Mark where platelets are.
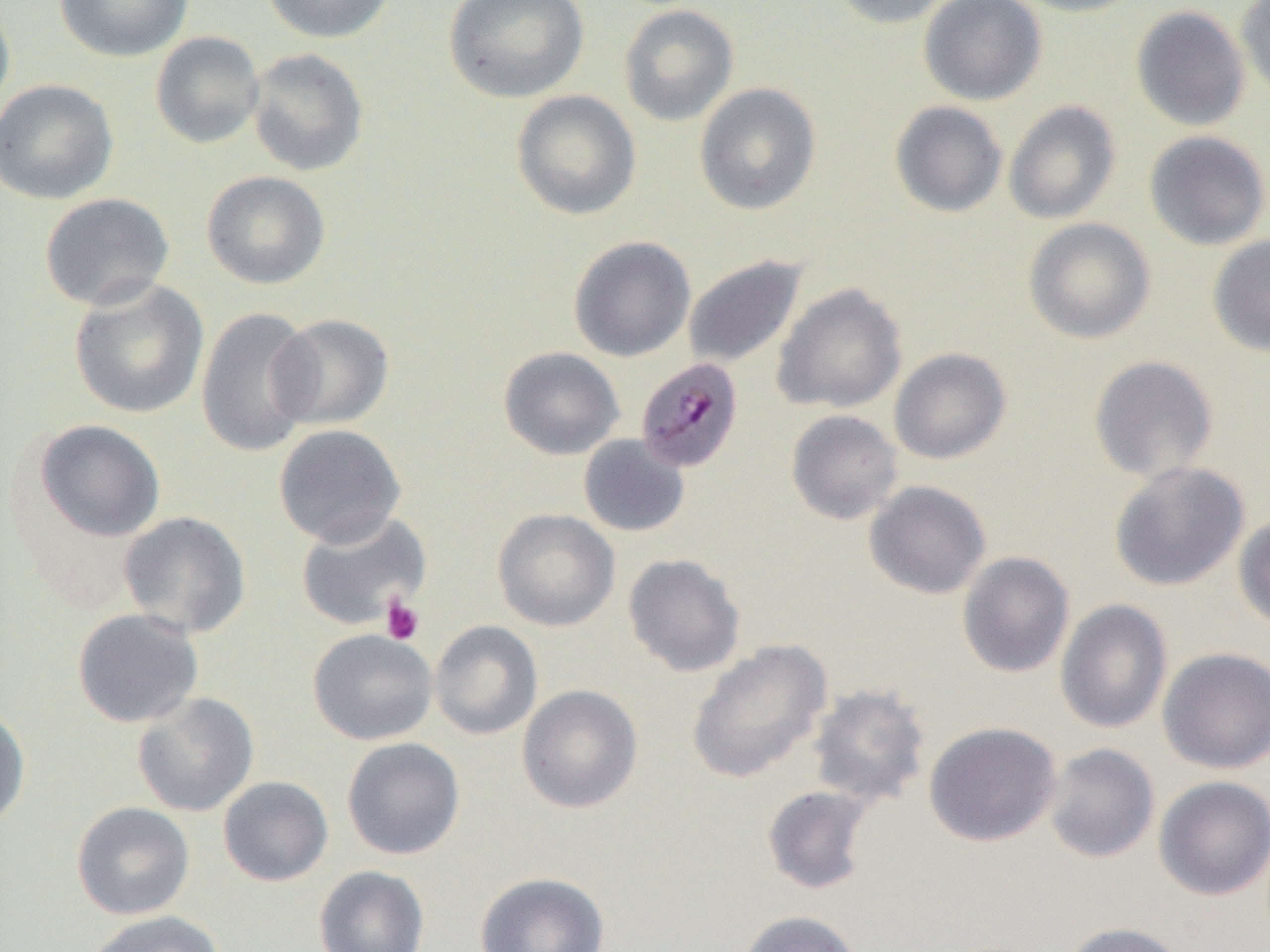

Approximate bounding boxes as (x1, y1, x2, y2) in pixels.
Platelets: (380, 596, 425, 645).

slide-level diagnosis = Plasmodium malariae
image size = 1270×952 pixels
preparation = thin blood smear
Plasmodium malariae-infected red blood cell locations = approximate bounding boxes as (x1, y1, x2, y2) in pixels: (635, 356, 744, 473)
uninfected red blood cell locations = approximate bounding boxes as (x1, y1, x2, y2) in pixels: (55, 0, 194, 62), (260, 0, 398, 44), (443, 0, 589, 104), (829, 0, 958, 29), (918, 0, 1047, 105), (1008, 0, 1147, 17), (1235, 0, 1270, 102), (0, 1, 15, 123), (618, 4, 739, 127), (1131, 6, 1250, 131), (150, 31, 265, 149), (246, 47, 370, 177), (0, 79, 118, 205), (694, 82, 821, 215), (511, 90, 641, 221), (1003, 100, 1121, 225), (890, 101, 1008, 218), (1144, 130, 1270, 251), (201, 170, 330, 290), (39, 193, 175, 311), (1023, 218, 1156, 344), (1207, 235, 1270, 357), (568, 236, 695, 362), (683, 255, 807, 370), (68, 277, 210, 419), (771, 282, 908, 414), (195, 307, 317, 457), (268, 314, 394, 431), (498, 346, 624, 460), (889, 347, 1012, 465), (1088, 354, 1220, 483), (785, 409, 903, 525), (34, 419, 166, 542), (273, 424, 406, 547), (578, 434, 690, 538), (1109, 460, 1249, 591), (864, 480, 992, 600), (493, 508, 620, 631), (118, 511, 251, 638), (296, 511, 432, 632), (1233, 514, 1270, 632), (957, 551, 1075, 678), (622, 553, 746, 677), (1055, 599, 1173, 734), (71, 608, 204, 728), (430, 620, 543, 740), (308, 628, 438, 745), (686, 638, 832, 783), (1157, 647, 1270, 774), (517, 684, 643, 813), (806, 684, 931, 808), (132, 692, 259, 817), (0, 701, 31, 831), (923, 721, 1062, 847), (342, 737, 465, 860), (1042, 743, 1160, 864), (1153, 775, 1270, 901), (218, 776, 333, 887), (762, 785, 875, 895), (71, 801, 194, 920), (314, 865, 430, 952), (474, 871, 610, 952), (735, 909, 866, 952), (84, 910, 226, 952), (1059, 921, 1189, 952)
field of view = one of a larger specimen
magnification = 1000x
modality = optical microscopy